Locate every Plasmodium parasite and identify its life-cycle stage.
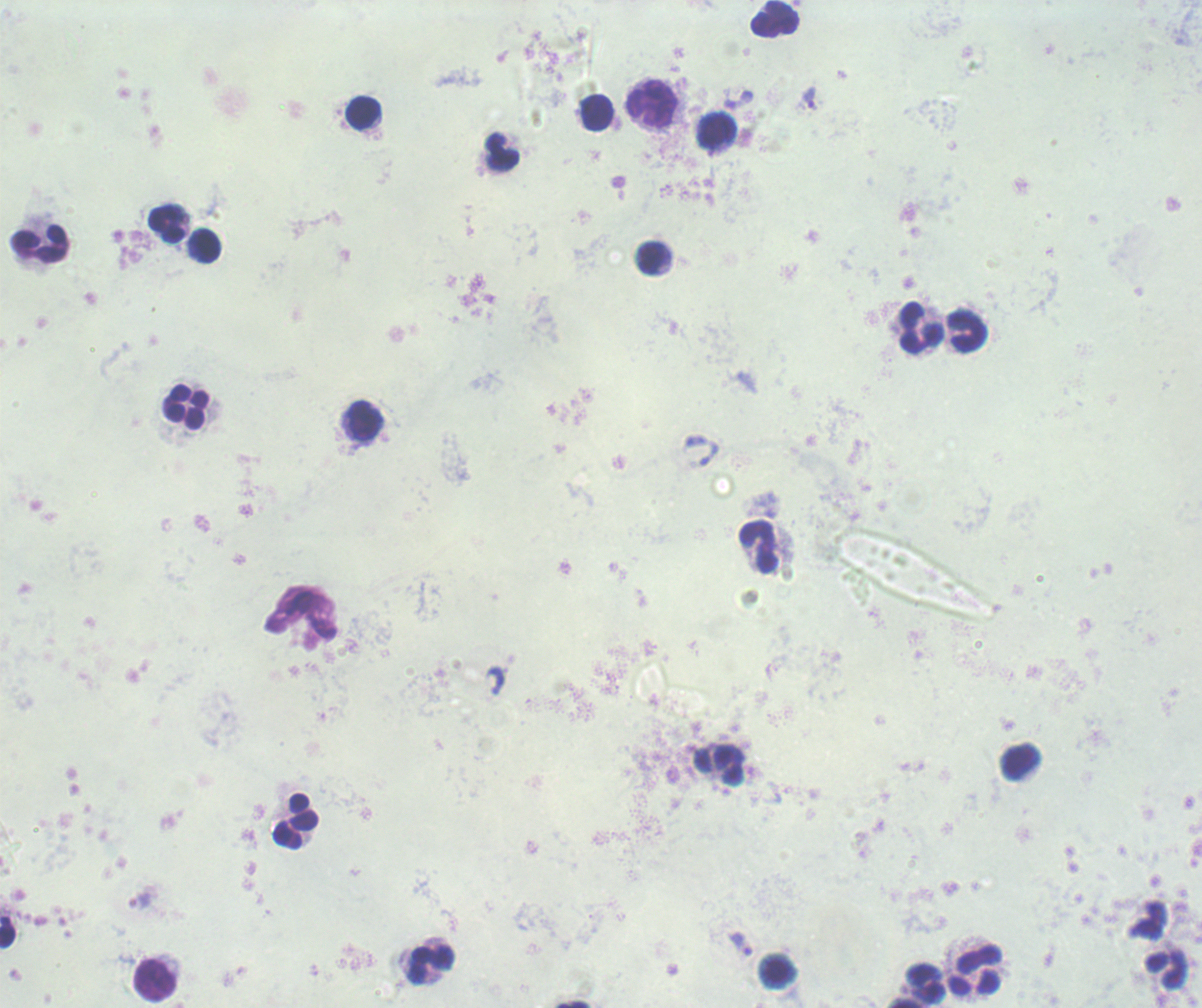

Approximate centers as [x, y] in pixels.
Trophozoites: [810, 99], [741, 944].
No schizont or gametocyte forms observed.

Approximate centers as [x, y] in pixels. Leukocyte locations: [774, 18], [651, 103], [595, 112], [363, 113], [717, 132], [502, 152], [166, 223], [39, 244], [208, 246], [653, 258], [920, 328], [968, 332], [186, 407], [365, 420], [759, 547], [1020, 761], [717, 767], [297, 820], [7, 932], [430, 966], [975, 970], [1165, 971], [154, 980], [917, 985], [572, 1004]. Previously used in an actual diagnosis. Romanowsky stain. 100x magnification. Thick blood film. Background quality: unsatisfactory. Single field of view. Image is 1202×1008 pixels.